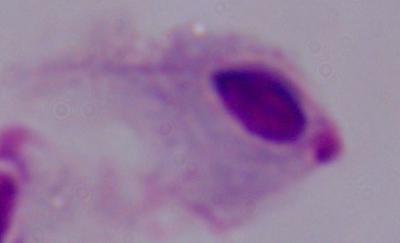

Summary:
  - Modality: photomicrograph
  - Identification: trichomonad
  - Magnification: 1000x